State which parasite is depicted.
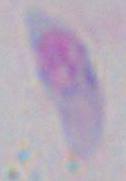
Toxoplasma gondii.

modality = photomicrograph
magnification = 1000x